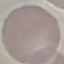
Result: no malaria parasites detected. Giemsa-stained preparation. Photographed with a smartphone camera at the microscope eyepiece. Automatically extracted cell patch, resized to 64 × 64 pixels. Thin smear of blood.